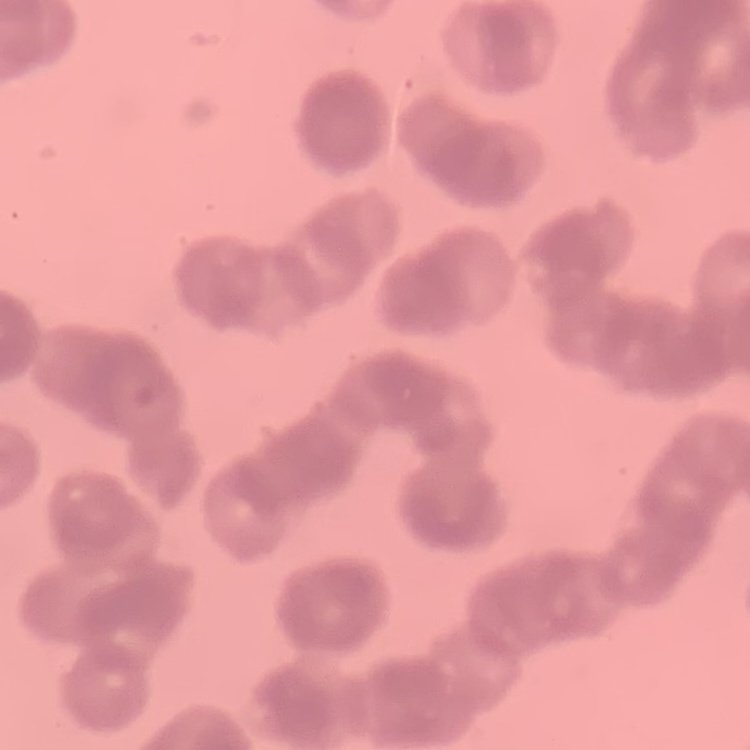

red blood cell morphology = rouleaux formation
stain = Field's or Giemsa
preparation = thin blood film
image type = square crop of a larger photomicrograph